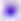
Summary:
  - Modality: photomicrograph
  - Identification: Toxoplasma gondii
  - Magnification: 400x